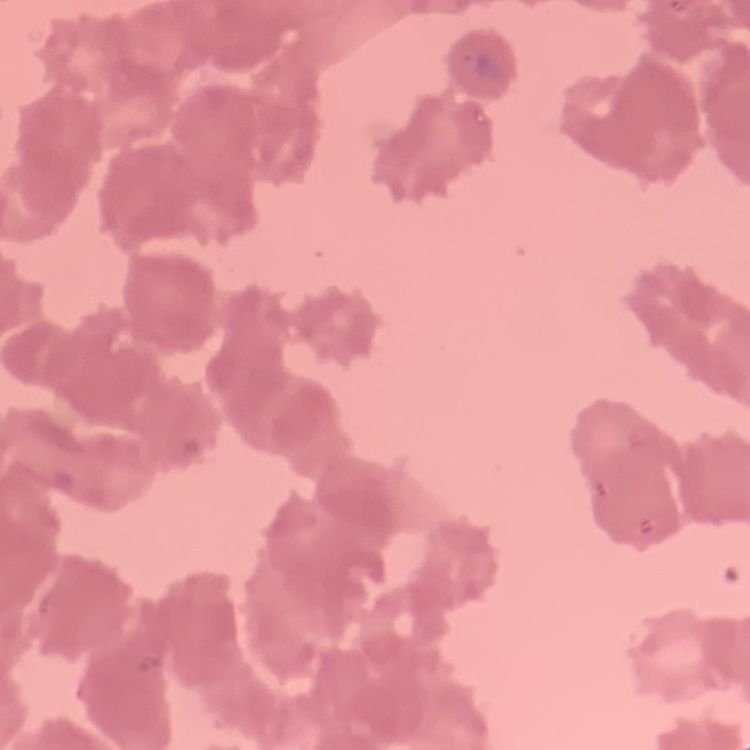
Summary:
  - Erythrocyte morphology: rouleaux formation
  - Image type: square crop of a larger photomicrograph
  - Preparation: thin blood smear
  - Stain: Field's or Giemsa